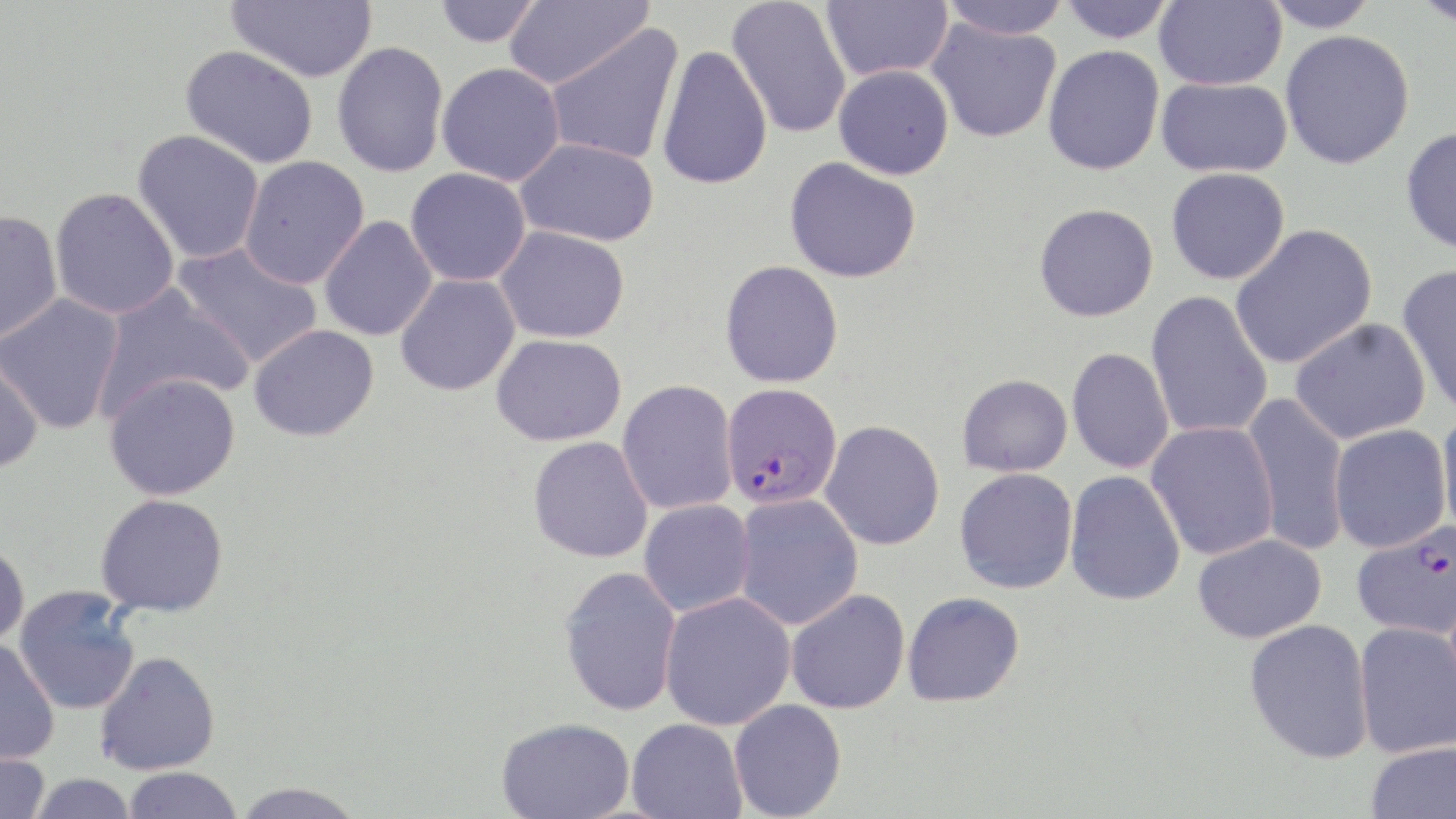
plasmodium_falciparum_infected_red_blood_cell_locations: 'approximate bounding boxes as [x1, y1, x2, y2] in pixels: [721, 382, 842, 509], [1352, 519, 1456, 640]'
slide_level_diagnosis: Plasmodium falciparum
image_size: 1456×819 pixels
preparation: thin blood smear
magnification: 1000x
modality: optical microscopy
stain: May-Grünwald-Giemsa
uninfected_red_blood_cell_locations: 'approximate bounding boxes as [x1, y1, x2, y2] in pixels: [227, 0, 377, 82], [504, 0, 653, 90], [726, 0, 852, 139], [822, 0, 953, 82], [939, 0, 1070, 40], [1057, 0, 1174, 43], [1154, 0, 1286, 90], [1259, 0, 1382, 32], [1413, 0, 1456, 29], [434, 1, 542, 48], [926, 18, 1061, 143], [544, 24, 684, 165], [1279, 30, 1415, 170], [332, 41, 449, 177], [656, 44, 773, 191], [180, 45, 319, 168], [1042, 45, 1164, 176], [436, 62, 566, 187], [834, 65, 954, 179], [1157, 77, 1293, 178], [1401, 126, 1456, 254], [132, 129, 264, 264], [515, 138, 660, 247], [239, 156, 369, 289], [785, 157, 921, 283], [1166, 167, 1290, 284], [405, 168, 531, 287], [50, 187, 180, 319], [1034, 203, 1159, 322], [0, 210, 63, 342], [319, 215, 437, 341], [1230, 224, 1378, 369], [495, 225, 630, 344], [172, 242, 323, 368], [720, 260, 844, 388], [1398, 263, 1456, 417], [395, 274, 520, 396], [91, 284, 253, 420], [1146, 290, 1273, 440], [0, 293, 125, 434], [1290, 317, 1431, 444], [248, 323, 379, 442], [491, 334, 626, 446], [1066, 347, 1175, 474], [0, 351, 44, 475], [104, 372, 241, 500], [957, 373, 1072, 477], [617, 380, 738, 515], [1241, 393, 1349, 554], [1436, 410, 1456, 540], [820, 420, 945, 550], [1146, 421, 1279, 560], [1329, 424, 1451, 552], [528, 437, 653, 563], [954, 467, 1078, 594], [1064, 470, 1185, 606], [95, 494, 229, 617], [733, 494, 863, 631], [639, 500, 755, 616], [1192, 533, 1327, 643], [0, 542, 30, 651], [558, 566, 682, 717], [14, 586, 142, 715], [786, 590, 910, 715], [902, 591, 1025, 707], [659, 592, 796, 730], [1244, 618, 1373, 763], [1354, 623, 1456, 758], [0, 640, 59, 765], [94, 650, 221, 775], [729, 699, 846, 819], [496, 717, 635, 819], [626, 717, 746, 819], [1366, 741, 1456, 819], [0, 749, 49, 819], [123, 767, 242, 819], [29, 773, 137, 818], [230, 782, 367, 818]'
field_of_view: single